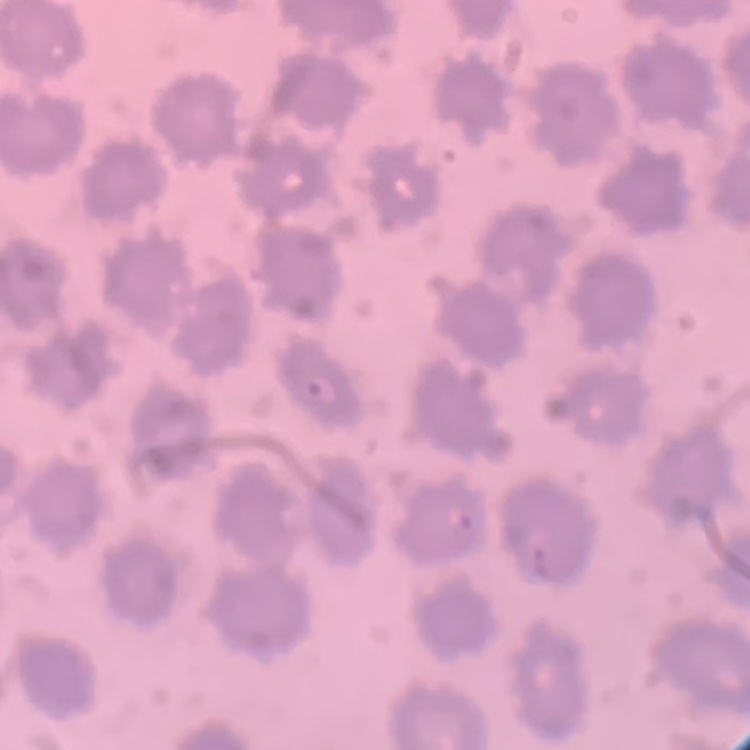
Summary:
  - Erythrocyte morphology: no rouleaux formation
  - Stain: Field's or Giemsa
  - Image type: one tile cut from a larger photomicrograph
  - Preparation: thin peripheral smear